Name the parasite shown.
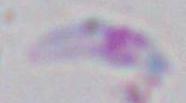
This is Toxoplasma gondii.

magnification = 1000x
modality = photomicrograph